Classify this cell by malaria status.
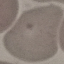
It is uninfected.

Photographed with a smartphone camera at the microscope eyepiece. Giemsa-stained preparation. Automatically extracted cell patch, resized to 64 × 64 pixels. Thin smear of blood.